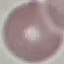
Result: negative for malaria parasites. Photographed with a smartphone camera at the microscope eyepiece. Thin blood film. Cell patch, automatically extracted from a larger field of view and resized to 64 × 64 pixels. Giemsa stain.